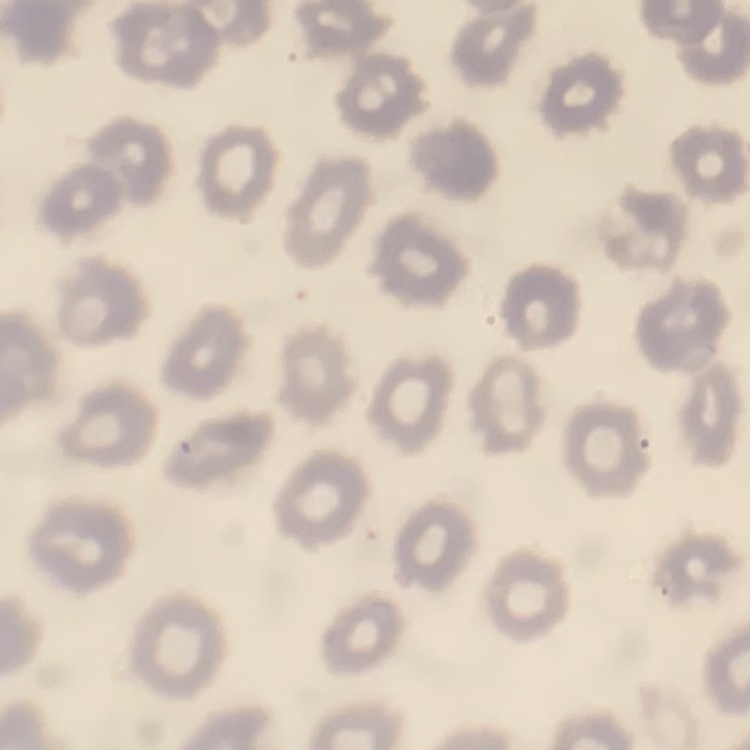

Summary:
  - Erythrocyte morphology: no rouleaux formation
  - Preparation: thin blood film
  - Image type: one tile cut from a larger photomicrograph
  - Stain: Field's or Giemsa